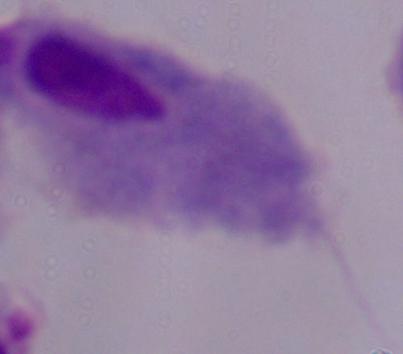

identification = trichomonad
modality = micrograph
magnification = 1000x